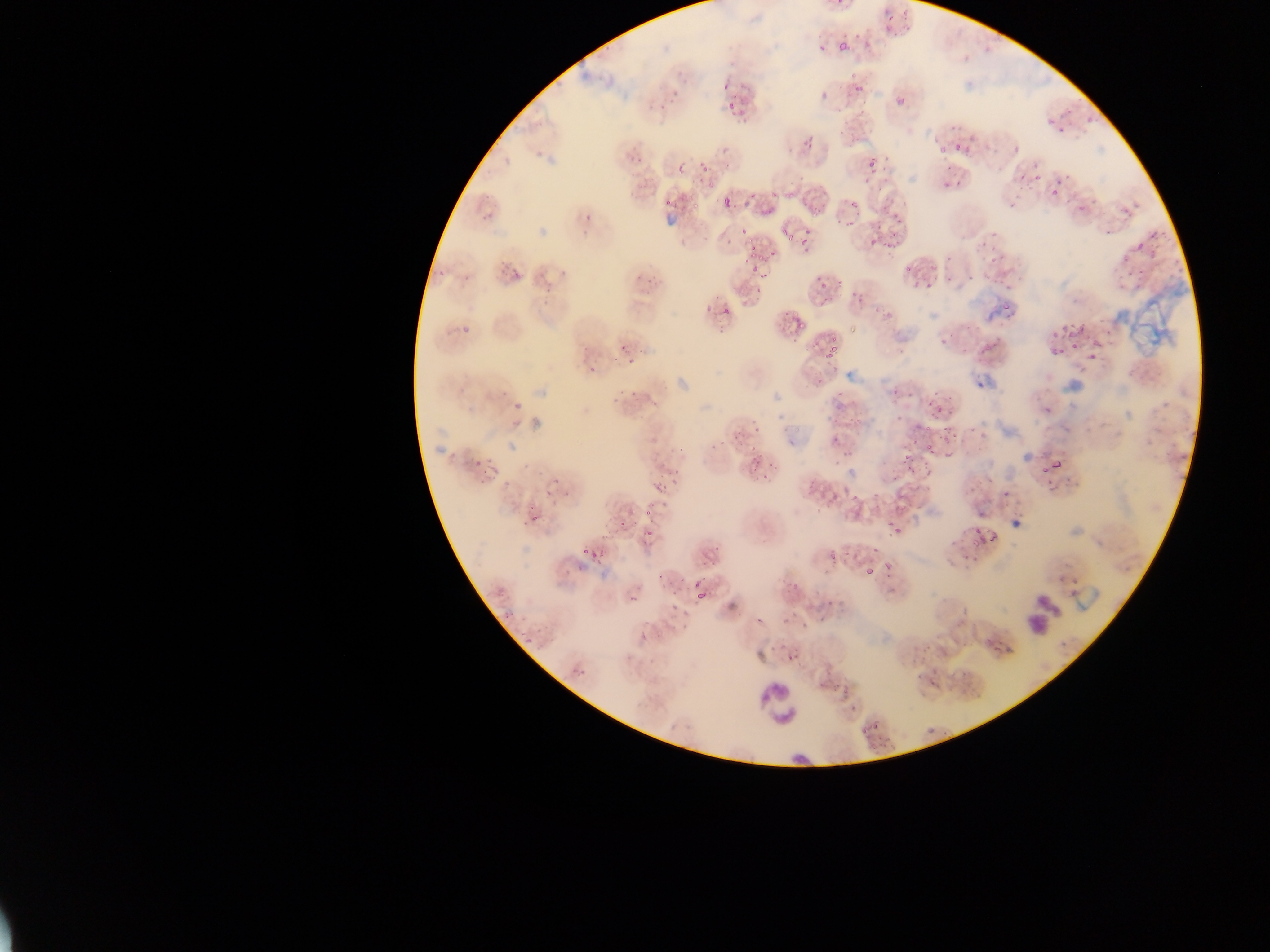
Approximate bounding boxes as left top right bottom in pixels.
Summary:
  - Leukocyte locations: 1015 588 1073 633; 755 683 802 727
  - Plasmodium parasite locations: 846 76 868 93; 721 82 729 91; 646 83 687 109; 721 93 745 112; 897 97 904 105; 988 132 1012 155; 792 134 812 150; 622 142 647 166; 954 143 969 156; 934 147 945 157; 696 149 714 173; 868 162 883 175; 678 164 686 173; 942 168 964 192; 1022 174 1037 189; 849 182 878 207; 775 187 796 200; 1048 187 1063 201; 687 189 698 214; 709 197 732 212; 665 199 673 207; 752 204 773 219; 807 206 824 220; 478 210 498 233; 584 214 591 222; 880 215 900 228; 982 224 1006 254; 866 227 887 249; 796 228 807 238; 778 234 799 249; 748 240 764 266; 980 246 1007 270; 938 257 953 281; 741 262 762 280; 900 262 918 277; 632 263 659 285; 502 268 522 284; 531 271 551 304; 812 274 829 290; 998 276 1009 286; 914 277 927 288; 854 278 865 304; 715 295 736 317; 880 300 895 320; 868 304 878 312; 997 306 1012 316; 452 311 474 342; 783 314 803 339; 930 323 954 348; 823 325 848 366; 1070 325 1080 333; 1051 328 1062 341; 806 333 827 358; 619 339 637 366; 1088 339 1101 358; 1066 340 1078 357; 1048 347 1059 359; 588 365 597 374; 834 372 858 403; 612 377 638 400; 889 380 906 393; 938 395 949 410; 506 396 525 412; 846 402 879 421; 920 406 932 417; 825 408 843 427; 907 422 917 431; 733 423 750 441; 941 426 951 441; 826 427 849 456; 923 438 936 457; 900 445 919 467; 469 449 492 466; 745 450 767 467; 1053 457 1064 469; 1035 464 1048 475; 847 473 871 501; 677 475 696 489; 805 478 823 495; 543 479 558 500; 1002 480 1019 500; 651 481 668 492; 821 483 846 507; 890 488 913 512; 965 489 982 508; 642 497 659 516; 520 510 537 525; 611 515 624 533; 890 520 903 533; 641 522 654 542; 971 528 990 552; 581 539 598 560; 706 539 723 553; 954 546 962 561; 826 547 842 560; 651 557 676 591; 865 560 875 575; 693 564 708 590; 777 567 801 592; 673 579 688 603; 618 581 636 598; 779 588 810 622; 817 588 843 614; 698 593 708 602; 958 604 973 629; 987 622 1005 645; 777 635 799 664; 839 675 859 692; 920 721 940 739; 859 723 874 741
  - Preparation: thin blood film
  - Country: Ghana
  - Capture: mobile-phone photograph through a microscope
  - Field of view: single
  - Image size: 1270×952 pixels